Classify this cell by malaria status.
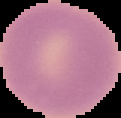
It is uninfected.

Image is 121×118 pixels. From a thin blood film. Cell region segmented out of the field of view; the surrounding area is masked to black.